Identify the parasite.
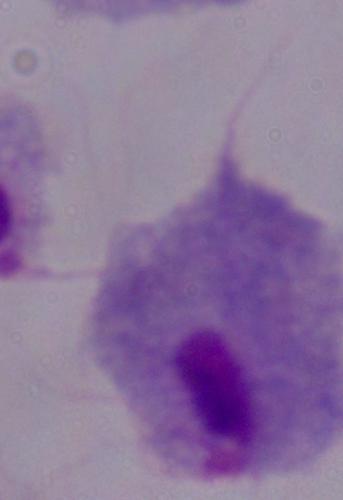

A trichomonad.

Summary:
  - Magnification: 1000x
  - Modality: micrograph